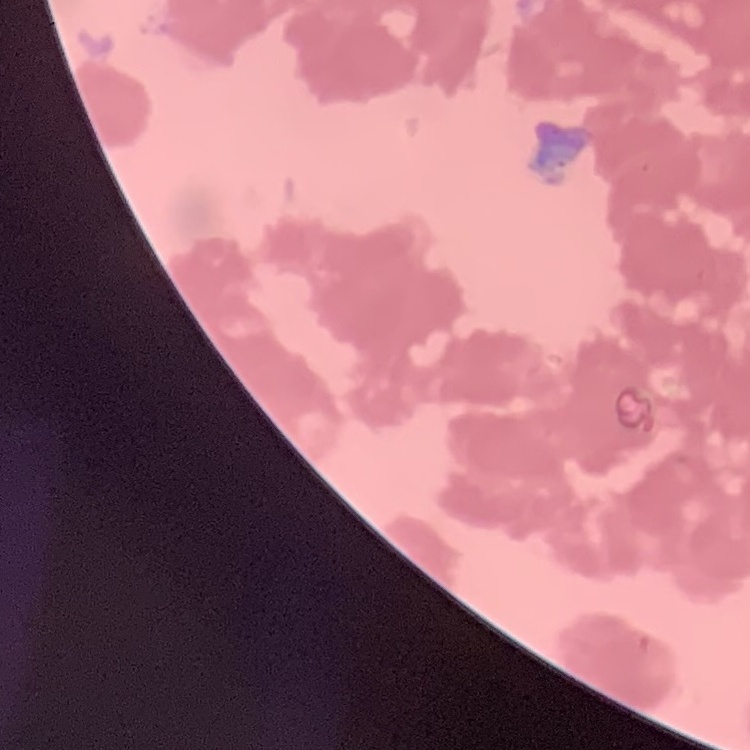
The red blood cells exhibit rouleaux formation. Thin peripheral smear. Field's or Giemsa stain. One tile cut from a larger photomicrograph.